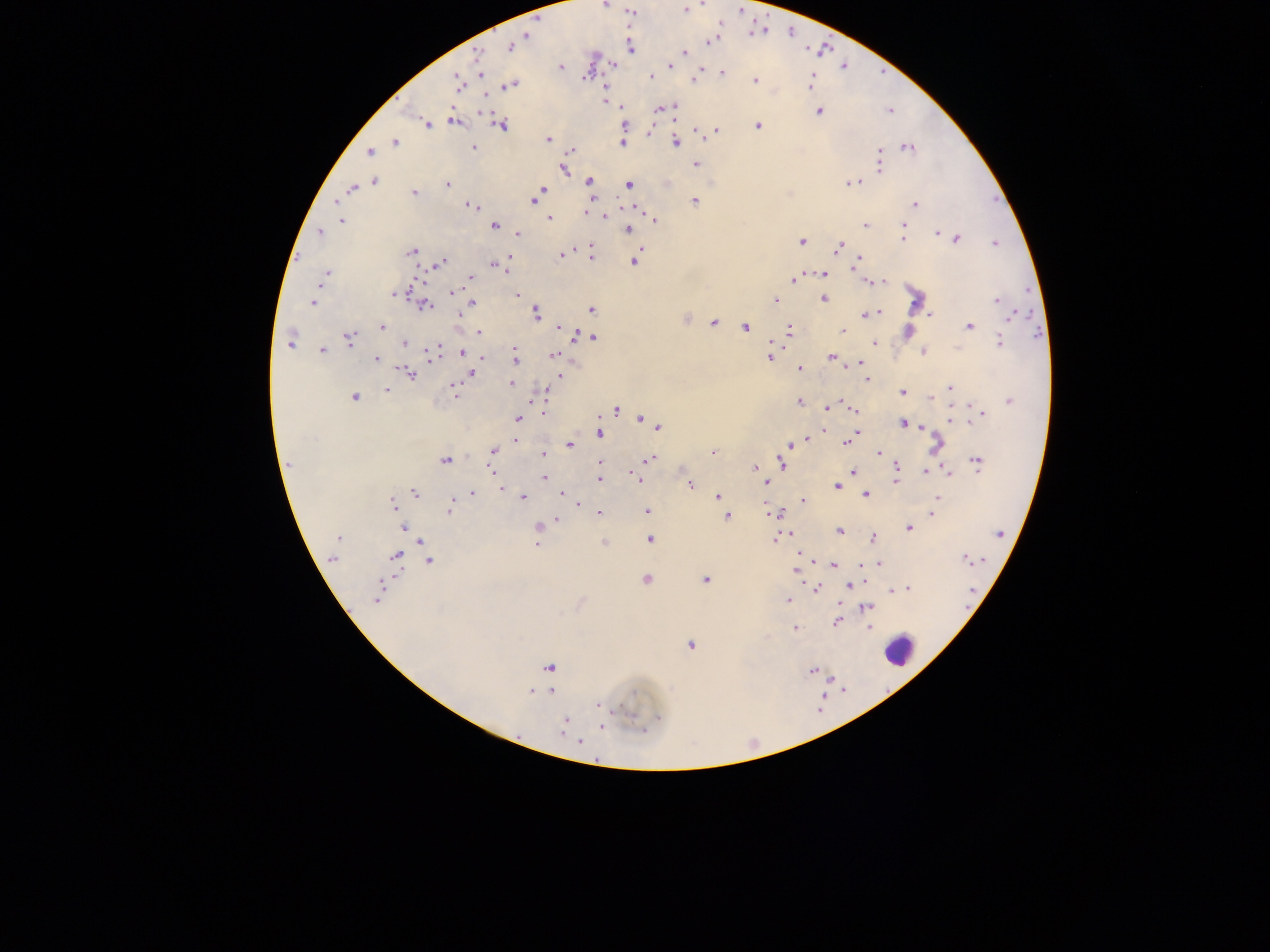
country = Ghana
preparation = thick blood smear
image size = 1270×952 pixels
leukocyte locations = approximate centers as [x, y] in pixels: [899, 649]
malaria parasite locations = approximate centers as [x, y] in pixels: [604, 4], [630, 11], [751, 34], [527, 35], [710, 40], [509, 46], [630, 48], [685, 51], [476, 54], [613, 65], [560, 66], [671, 66], [843, 67], [720, 73], [481, 75], [651, 75], [695, 78], [810, 79], [754, 80], [458, 81], [509, 85], [606, 88], [604, 93], [605, 101], [622, 107], [660, 108], [819, 110], [889, 110], [674, 111], [481, 112], [453, 120], [426, 123], [757, 124], [501, 125], [696, 130], [717, 131], [649, 132], [548, 139], [394, 142], [622, 142], [676, 142], [906, 147], [473, 148], [570, 149], [369, 152], [878, 152], [879, 162], [694, 163], [562, 169], [374, 180], [588, 180], [850, 183], [447, 184], [629, 185], [351, 188], [543, 188], [414, 193], [537, 197], [589, 197], [533, 200], [693, 201], [337, 202], [915, 204], [471, 205], [475, 207], [585, 212], [339, 213], [605, 215], [548, 218], [342, 220], [654, 220], [495, 225], [865, 225], [904, 226], [628, 229], [319, 232], [937, 233], [517, 234], [901, 239], [955, 239], [802, 241], [995, 244], [589, 246], [838, 247], [412, 251], [560, 255], [591, 257], [859, 259], [508, 260], [634, 261], [856, 262], [439, 263], [493, 264], [501, 267], [506, 270], [823, 273], [325, 274], [471, 277], [792, 279], [867, 281], [882, 281], [453, 292], [394, 293], [516, 295], [822, 298], [997, 299], [774, 300], [313, 302], [473, 304], [424, 305], [591, 309], [878, 312], [536, 313], [865, 314], [930, 314], [1010, 317], [684, 320], [713, 322], [968, 326], [381, 327], [558, 327], [745, 327], [843, 330], [479, 331], [567, 331], [789, 332], [577, 334], [591, 337], [349, 338], [290, 342], [404, 343], [874, 343], [999, 343], [514, 349], [322, 350], [923, 351], [431, 352], [462, 352], [553, 354], [481, 355], [770, 357], [831, 357], [514, 358], [376, 359], [861, 362], [847, 367], [798, 369], [471, 372], [410, 373], [560, 376], [866, 378], [511, 383], [454, 385], [950, 387], [385, 391], [901, 391], [454, 392], [544, 392], [354, 397], [930, 398], [1010, 400], [797, 402], [828, 407], [854, 409], [615, 410], [543, 413], [982, 415], [640, 417], [519, 418], [949, 420], [902, 423], [921, 426], [657, 427], [822, 430], [857, 430], [599, 434], [855, 434], [808, 437], [516, 439], [803, 441], [846, 442], [569, 444], [790, 445], [935, 445], [492, 451], [713, 453], [542, 454], [878, 454], [648, 459], [445, 461], [977, 462], [600, 463], [781, 464], [896, 464], [288, 465], [755, 467], [492, 470], [947, 471], [924, 472], [632, 473], [853, 473], [543, 478], [599, 479], [637, 479], [895, 481], [765, 482], [689, 484], [835, 485], [501, 488], [413, 493], [472, 494], [561, 494], [865, 494], [937, 496], [522, 497], [717, 497], [802, 501], [575, 503], [766, 503], [392, 505], [451, 507], [646, 511], [598, 512], [768, 512], [932, 513], [780, 514], [725, 516], [557, 519], [538, 526], [403, 527], [908, 528], [839, 531], [999, 532], [789, 534], [338, 537], [872, 538], [649, 539], [418, 540], [773, 540], [604, 542], [537, 543], [799, 553], [396, 556], [964, 557], [332, 558], [428, 560], [811, 560], [878, 564], [833, 565], [796, 568], [645, 579], [705, 579], [848, 585], [815, 587], [909, 589], [892, 591], [378, 592], [787, 600], [866, 607], [836, 621], [868, 628], [795, 629], [690, 645], [550, 667], [813, 670], [530, 691], [551, 691], [597, 703], [566, 719], [563, 723], [601, 727], [561, 733], [579, 741]
capture = mobile-phone photograph through a microscope
field of view = single